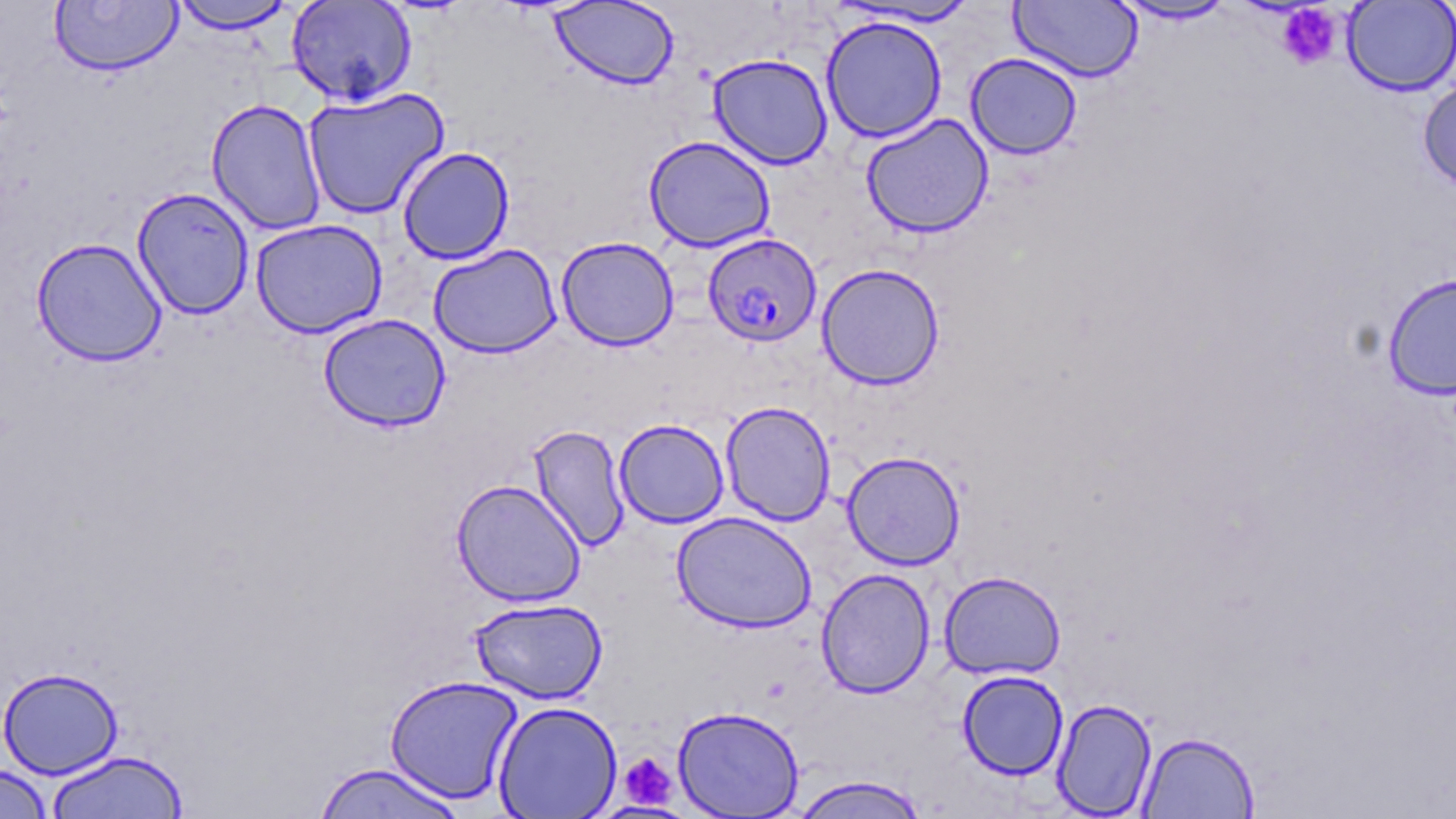
slide-level diagnosis = Plasmodium falciparum
uninfected red blood cell locations = approximate bounding boxes as named x1/y1/x2/y2 corners in pixels: (x1=170, y1=0, x2=295, y2=33), (x1=285, y1=0, x2=418, y2=106), (x1=1010, y1=0, x2=1142, y2=83), (x1=1342, y1=0, x2=1456, y2=96), (x1=49, y1=1, x2=183, y2=76), (x1=549, y1=1, x2=680, y2=90), (x1=833, y1=1, x2=981, y2=28), (x1=1111, y1=1, x2=1237, y2=25), (x1=821, y1=14, x2=948, y2=143), (x1=707, y1=52, x2=834, y2=170), (x1=965, y1=53, x2=1082, y2=159), (x1=1417, y1=76, x2=1456, y2=194), (x1=302, y1=87, x2=450, y2=220), (x1=206, y1=98, x2=327, y2=236), (x1=861, y1=113, x2=994, y2=238), (x1=644, y1=135, x2=776, y2=252), (x1=397, y1=146, x2=515, y2=265), (x1=132, y1=187, x2=255, y2=320), (x1=250, y1=219, x2=387, y2=338), (x1=556, y1=236, x2=679, y2=351), (x1=31, y1=237, x2=166, y2=367), (x1=428, y1=243, x2=562, y2=358), (x1=817, y1=263, x2=945, y2=390), (x1=1382, y1=272, x2=1456, y2=400), (x1=318, y1=313, x2=451, y2=432), (x1=720, y1=401, x2=836, y2=526), (x1=614, y1=418, x2=729, y2=528), (x1=528, y1=425, x2=631, y2=551), (x1=842, y1=450, x2=966, y2=570), (x1=451, y1=479, x2=586, y2=607), (x1=671, y1=510, x2=817, y2=633), (x1=816, y1=568, x2=936, y2=698), (x1=939, y1=570, x2=1066, y2=680), (x1=469, y1=598, x2=608, y2=705), (x1=0, y1=666, x2=124, y2=779), (x1=957, y1=670, x2=1069, y2=780), (x1=384, y1=674, x2=523, y2=805), (x1=1051, y1=697, x2=1158, y2=818), (x1=493, y1=700, x2=622, y2=818), (x1=672, y1=705, x2=805, y2=817), (x1=1137, y1=731, x2=1259, y2=818), (x1=44, y1=750, x2=189, y2=818), (x1=312, y1=761, x2=469, y2=819), (x1=0, y1=764, x2=54, y2=819), (x1=788, y1=774, x2=930, y2=819)
modality = optical microscopy
stain = May-Grünwald-Giemsa
field of view = one of a larger specimen
platelet locations = approximate bounding boxes as named x1/y1/x2/y2 corners in pixels: (x1=1276, y1=4, x2=1342, y2=71), (x1=619, y1=752, x2=677, y2=808)
image size = 1456×819 pixels
preparation = thin blood smear
Plasmodium falciparum-infected red blood cell locations = approximate bounding boxes as named x1/y1/x2/y2 corners in pixels: (x1=707, y1=232, x2=826, y2=346)
magnification = 1000x